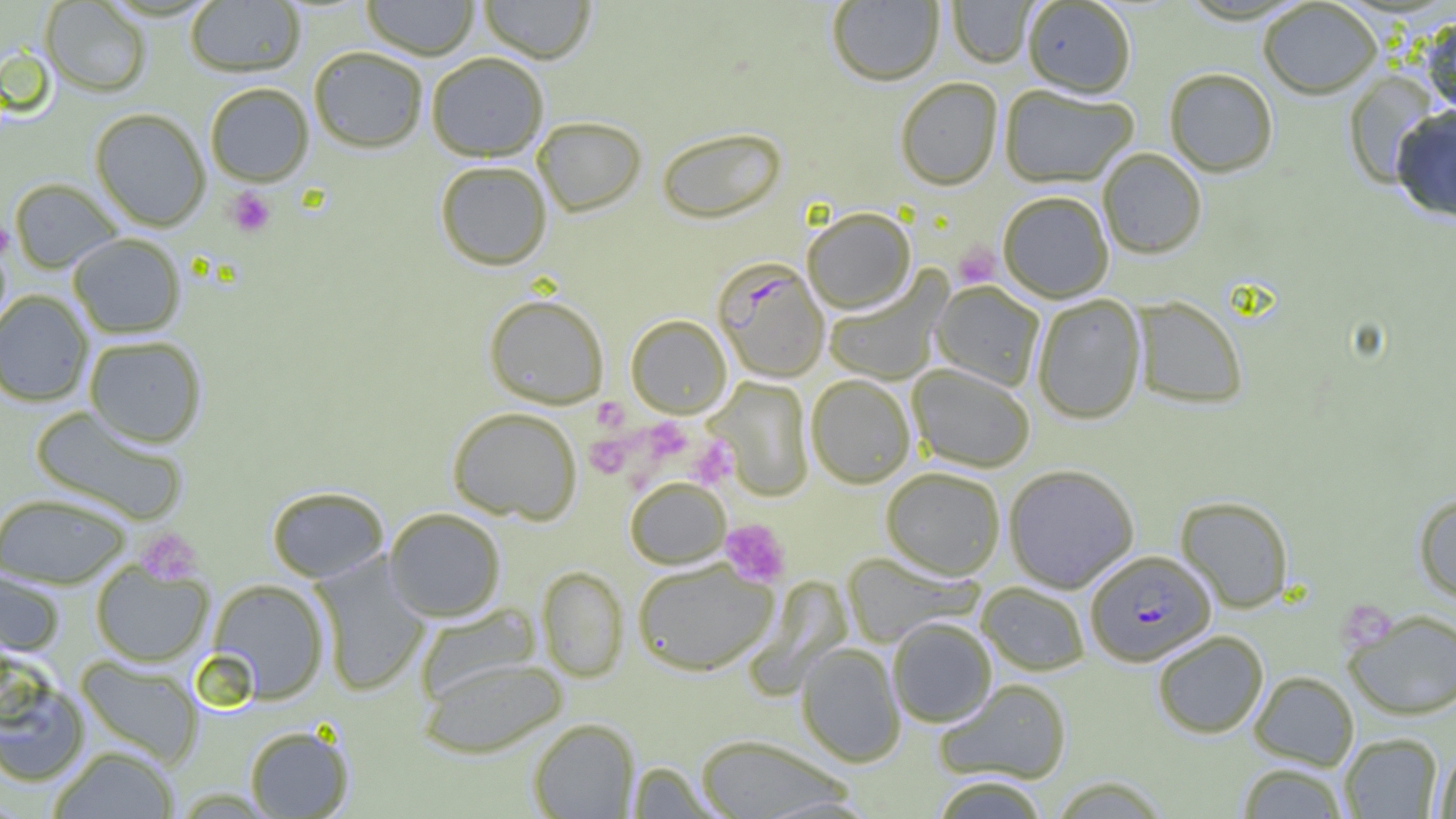 Approximate bounding boxes as (x1,y1)-(x2,y2) corner pairs in pixels. Uninfected red blood cell locations: (361,0)-(480,60), (478,0)-(596,63), (1021,0)-(1136,98), (39,1)-(152,97), (185,1)-(305,77), (827,1)-(945,86), (947,1)-(1036,67), (1258,1)-(1382,99), (1421,16)-(1456,118), (308,46)-(429,153), (425,52)-(549,161), (1164,68)-(1278,177), (1342,70)-(1442,188), (895,77)-(1003,190), (205,82)-(314,186), (999,85)-(1137,188), (1391,106)-(1456,223), (90,108)-(211,231), (532,116)-(647,216), (656,126)-(787,224), (1097,148)-(1207,259), (434,160)-(552,270), (9,178)-(122,273), (997,191)-(1114,302), (802,207)-(916,314), (68,233)-(186,338), (822,271)-(950,385), (932,281)-(1044,391), (0,290)-(94,407), (483,293)-(609,408), (1032,294)-(1146,424), (1132,296)-(1247,409), (625,314)-(732,418), (83,335)-(208,447), (907,364)-(1035,473), (805,374)-(915,488), (707,377)-(815,500), (30,406)-(189,525), (447,406)-(583,524), (1003,463)-(1139,593), (880,467)-(1006,579), (625,477)-(731,568), (266,485)-(389,582), (0,492)-(131,588), (1414,493)-(1456,602), (1175,495)-(1294,613), (384,507)-(506,622), (311,552)-(432,697), (842,552)-(981,647), (631,559)-(779,675), (90,560)-(214,667), (537,566)-(629,682), (0,568)-(65,657), (207,578)-(330,703), (976,582)-(1090,676), (413,603)-(542,705), (1345,608)-(1456,720), (887,618)-(997,727), (1152,630)-(1268,738), (795,643)-(906,767), (75,655)-(203,768), (417,656)-(568,759), (1,669)-(91,788), (1249,670)-(1359,771), (935,678)-(1072,784), (528,718)-(640,818), (244,724)-(354,818), (1339,733)-(1442,818), (695,734)-(853,819), (1434,744)-(1456,819), (48,745)-(179,818), (627,761)-(719,819), (1237,763)-(1349,818), (929,776)-(1050,818). Plasmodium falciparum-infected red blood cell locations: (713,258)-(830,383), (1086,549)-(1216,666). Platelet locations: (226,187)-(276,238), (0,221)-(13,259), (953,243)-(1000,288), (592,397)-(629,431), (643,417)-(692,461), (585,434)-(631,478), (688,436)-(737,487), (719,519)-(792,588), (136,527)-(203,585), (1337,601)-(1396,652). Slide-level diagnosis: Plasmodium falciparum. Image is 1456×819 pixels. Thin blood film. Captured at 1000x magnification. One field of a larger specimen. Optical microscopy.